Report the malaria status.
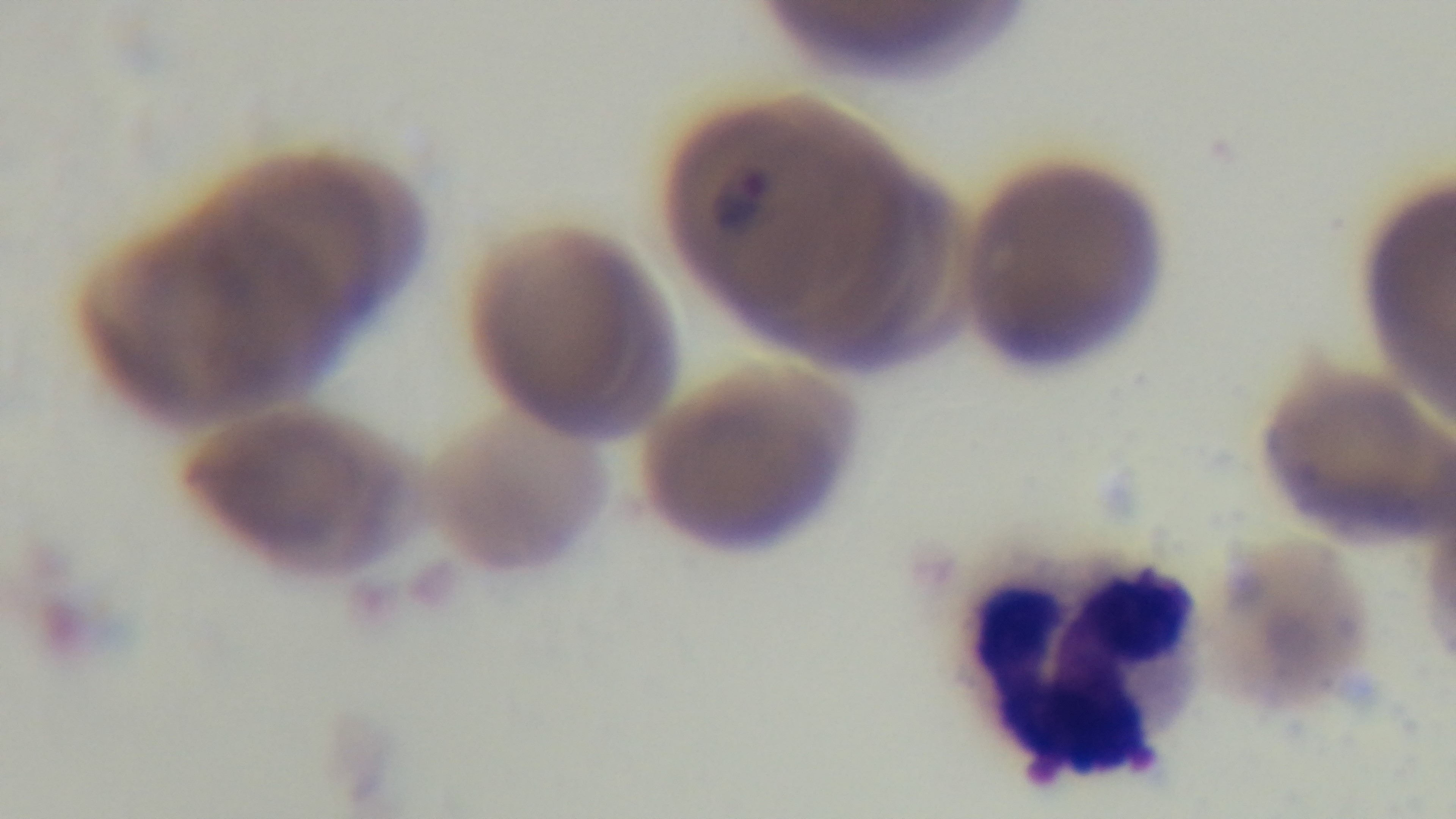
Positive.

Summary:
  - Field of view: single
  - Objective: 100x oil immersion
  - Preparation: thin blood film
  - Capture: mounted 4K digital camera
  - Stain: Giemsa
  - Modality: light microscopy